Mark where platelets are.
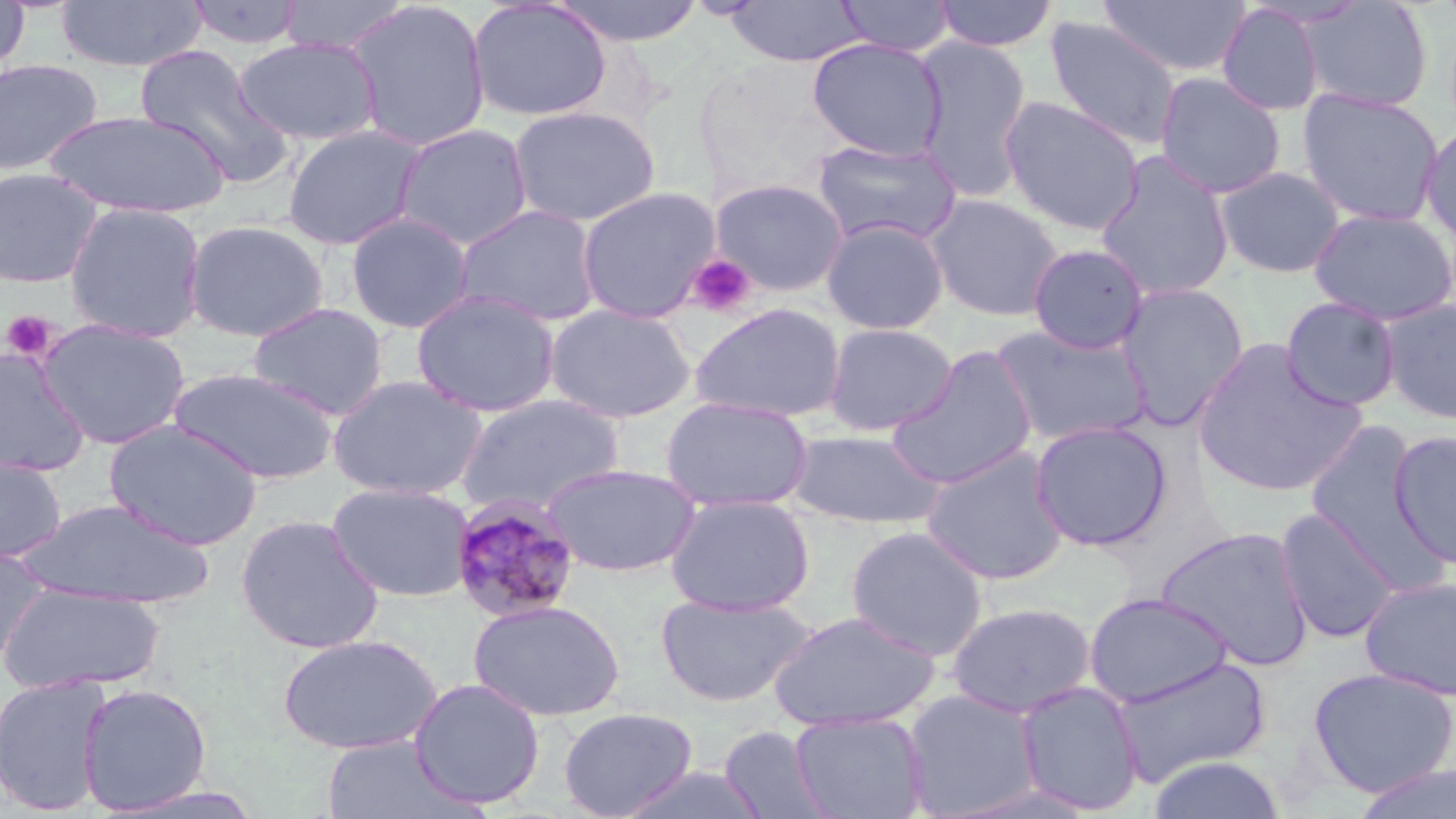
Approximate bounding boxes as (x1,y1)-(x2,y2) corner pairs in pixels.
Platelets: (686,253)-(756,317), (2,311)-(55,360).

Uninfected red blood cell locations: (278,0)-(411,56), (550,0)-(705,46), (834,0)-(956,56), (932,0)-(1058,52), (1099,0)-(1250,79), (0,1)-(31,82), (54,1)-(207,72), (185,1)-(305,49), (344,1)-(492,152), (467,1)-(612,122), (725,1)-(867,66), (1298,1)-(1434,113), (1217,3)-(1325,117), (1044,16)-(1180,150), (233,36)-(382,146), (807,38)-(947,161), (912,39)-(1032,201), (135,43)-(292,189), (0,58)-(103,176), (1153,71)-(1287,199), (1297,87)-(1446,228), (999,96)-(1145,236), (508,105)-(661,226), (43,110)-(228,219), (1420,120)-(1456,250), (394,123)-(533,250), (282,124)-(427,250), (810,138)-(963,248), (1094,152)-(1234,301), (1214,166)-(1345,279), (0,167)-(103,288), (710,179)-(848,296), (576,186)-(720,324), (924,192)-(1065,321), (64,202)-(207,342), (454,204)-(604,326), (1308,207)-(1456,325), (345,211)-(474,334), (820,218)-(949,335), (183,219)-(330,342), (1027,243)-(1149,354), (1115,282)-(1249,430), (411,289)-(561,417), (1279,297)-(1402,412), (1378,298)-(1456,426), (247,302)-(389,420), (689,302)-(847,423), (543,303)-(699,423), (37,319)-(190,449), (823,323)-(957,436), (991,323)-(1152,448), (1190,339)-(1369,497), (886,346)-(1039,490), (0,348)-(92,477), (168,366)-(338,484), (327,374)-(487,500), (455,393)-(626,514), (661,396)-(813,513), (104,419)-(264,551), (1029,419)-(1173,551), (1300,420)-(1442,579), (788,428)-(943,529), (1388,428)-(1456,570), (921,445)-(1070,586), (0,454)-(67,563), (540,463)-(700,576), (327,481)-(476,602), (665,493)-(815,616), (16,497)-(217,610), (1274,506)-(1401,644), (236,514)-(385,655), (846,524)-(989,661), (1156,525)-(1315,671), (0,546)-(48,669), (1359,575)-(1456,701), (0,582)-(165,694), (1084,591)-(1233,707), (655,592)-(816,707), (468,599)-(625,721), (946,601)-(1098,718), (767,610)-(939,730), (276,634)-(441,755), (1109,654)-(1273,786), (1307,666)-(1456,797), (0,673)-(111,816), (408,677)-(546,810), (1014,680)-(1145,815), (77,682)-(213,815), (901,688)-(1044,817), (558,706)-(698,818), (790,710)-(929,819), (719,726)-(833,819), (320,735)-(475,819), (1146,754)-(1288,819), (1349,763)-(1456,818), (616,765)-(770,819), (943,780)-(1100,818). Plasmodium malariae-infected red blood cell locations: (449,495)-(582,624). Slide-level diagnosis: Plasmodium malariae. Single field of view. 1000x magnification. Image is 1456×819 pixels. Light microscopy. May-Grünwald-Giemsa stain. Thin blood film.